Report the malaria status of this cell.
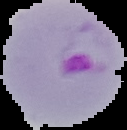
It is parasitized.

From a thin blood smear. Image is 127×130 pixels. Segmented cell region on a black background.